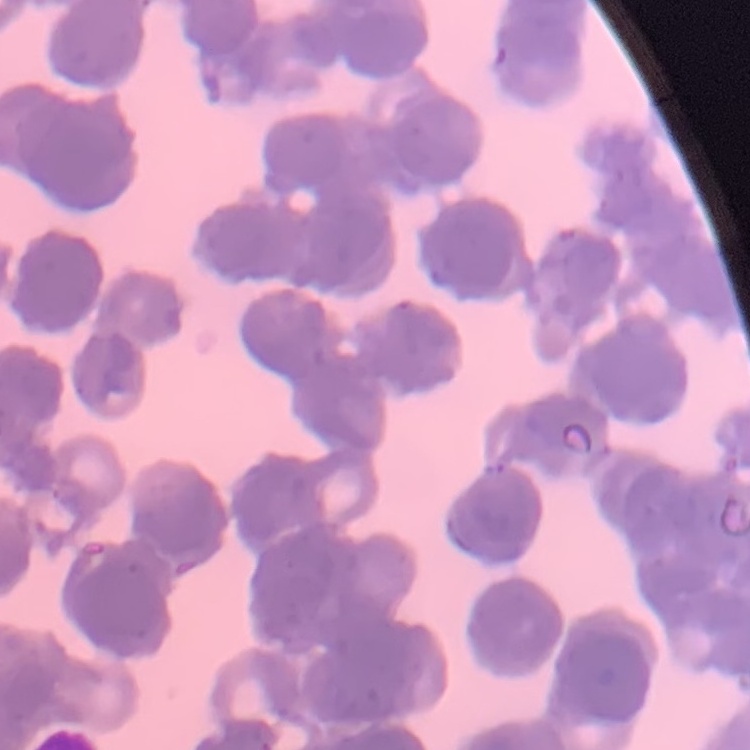
The red blood cells show rouleaux formation. Stained with either Field's or Giemsa. One tile cut from a larger photomicrograph. Thin blood smear.